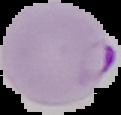
malaria status = parasitized
image type = segmented cell region with the area outside set to black
preparation = thin blood smear
image size = 121×115 pixels